Describe the morphology of the red blood cells.
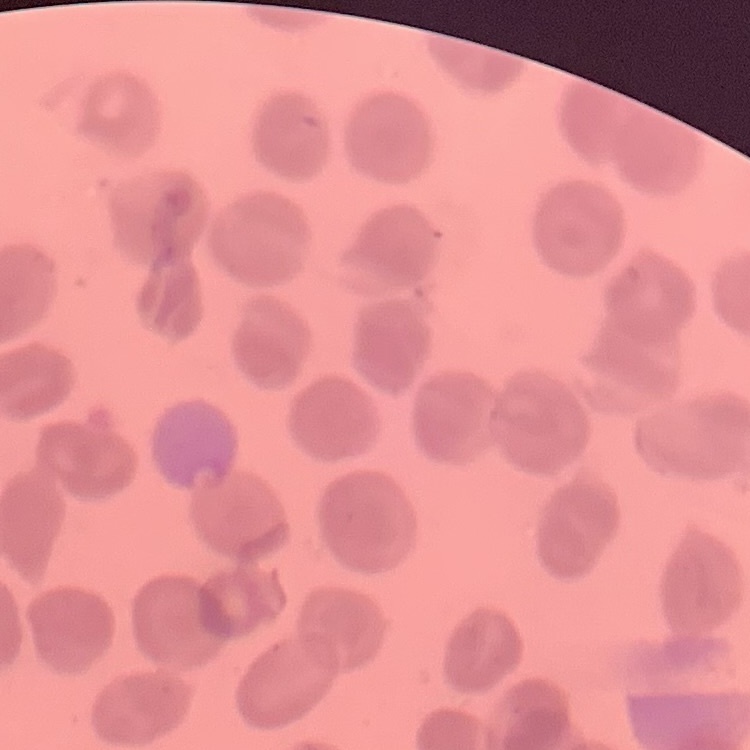
They show no rouleaux formation.

Field's or Giemsa stain. Thin blood smear. One tile cut from a larger photomicrograph.